Assess this cell for malaria.
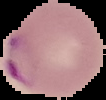
Parasitized.

image_size: 106×100 pixels
preparation: thin blood film
image_type: cell region segmented out of the field of view; surrounding area masked to black